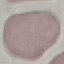

result = negative for malaria parasites
image type = cell patch, automatically extracted from a larger field of view and resized to 64 × 64 pixels
capture = smartphone through the microscope eyepiece
preparation = thin blood film
stain = Giemsa